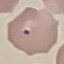
malaria status = parasitized
image type = automatically extracted cell patch, resized to 64 × 64 pixels
stain = Giemsa
preparation = thin blood film
capture = smartphone camera at the microscope eyepiece